Locate and identify every blood parasite.
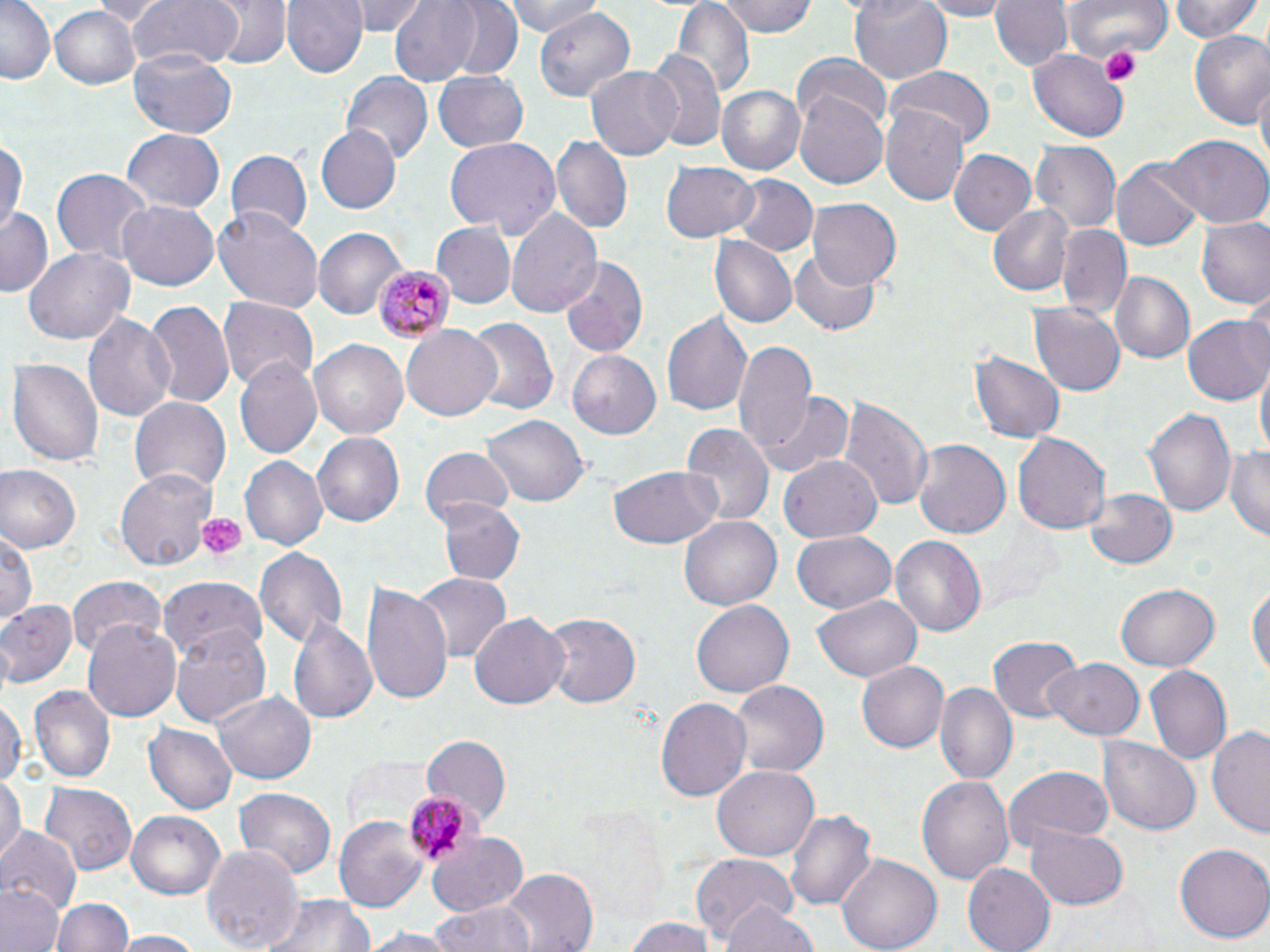

Approximate bounding boxes as (x1, y1, x2, y2) in pixels.
Plasmodium malariae-infected red blood cells: (377, 263, 453, 343), (402, 794, 477, 867).
No Plasmodium falciparum, Plasmodium ovale, Plasmodium vivax, Babesia divergens, or Trypanosoma brucei observed.

Platelet locations: (1100, 45, 1142, 86), (196, 511, 247, 563). Uninfected red blood cell locations: (1, 0, 53, 84), (88, 0, 170, 25), (124, 0, 240, 75), (205, 0, 289, 71), (283, 0, 368, 78), (353, 0, 428, 34), (388, 0, 485, 86), (441, 0, 526, 80), (503, 0, 601, 36), (715, 0, 819, 38), (848, 0, 953, 85), (911, 0, 1016, 18), (991, 0, 1072, 72), (1071, 0, 1171, 62), (1167, 0, 1264, 44), (671, 2, 755, 96), (528, 5, 632, 105), (49, 7, 140, 88), (1187, 27, 1270, 127), (1028, 47, 1128, 140), (128, 50, 236, 137), (647, 51, 725, 155), (792, 52, 889, 133), (585, 68, 682, 159), (888, 69, 994, 148), (433, 72, 527, 153), (341, 73, 432, 168), (1255, 79, 1270, 174), (715, 83, 808, 175), (794, 88, 890, 191), (882, 105, 970, 205), (314, 123, 401, 215), (122, 128, 224, 214), (1160, 134, 1270, 228), (0, 136, 26, 239), (443, 136, 560, 239), (553, 137, 631, 235), (1030, 140, 1121, 235), (949, 148, 1038, 236), (226, 149, 313, 238), (1111, 159, 1204, 248), (660, 162, 757, 243), (51, 168, 151, 263), (729, 175, 816, 255), (118, 200, 219, 292), (807, 200, 902, 291), (989, 203, 1075, 295), (214, 207, 325, 312), (0, 208, 52, 299), (507, 208, 602, 319), (1198, 217, 1270, 310), (432, 221, 514, 308), (1056, 223, 1129, 318), (313, 227, 406, 318), (710, 237, 795, 329), (24, 250, 132, 343), (788, 251, 882, 337), (558, 255, 649, 360), (1111, 272, 1195, 364), (143, 298, 236, 408), (217, 298, 320, 393), (1027, 302, 1126, 395), (659, 307, 753, 420), (82, 311, 176, 423), (1182, 313, 1270, 406), (465, 318, 560, 417), (402, 325, 503, 422), (731, 338, 818, 463), (309, 339, 409, 438), (567, 351, 661, 439), (7, 354, 103, 466), (971, 354, 1065, 442), (233, 356, 323, 462), (1255, 359, 1269, 465), (758, 393, 851, 476), (129, 395, 231, 497), (837, 395, 932, 515), (1143, 407, 1236, 517), (481, 410, 586, 504), (679, 422, 773, 531), (312, 432, 404, 528), (1012, 432, 1109, 535), (911, 440, 1010, 541), (1226, 446, 1270, 542), (420, 448, 515, 527), (780, 455, 882, 542), (240, 456, 327, 550), (609, 462, 726, 550), (0, 464, 81, 552), (115, 467, 216, 569), (1087, 486, 1178, 570), (435, 499, 525, 585), (679, 513, 785, 611), (2, 529, 37, 632), (792, 529, 898, 615), (892, 538, 986, 635), (254, 545, 347, 651), (412, 573, 511, 660), (68, 575, 167, 655), (158, 576, 269, 658), (1248, 576, 1269, 689), (361, 581, 455, 710), (1117, 582, 1219, 671), (811, 593, 923, 682), (0, 600, 77, 685), (691, 600, 792, 700), (469, 612, 568, 712), (542, 612, 640, 708), (289, 613, 381, 727), (82, 619, 182, 722), (168, 624, 273, 729), (989, 636, 1081, 723), (1048, 658, 1146, 741), (858, 660, 949, 753), (1143, 665, 1230, 765), (730, 679, 829, 779), (934, 683, 1018, 786), (29, 685, 116, 783), (213, 688, 317, 785), (0, 693, 24, 792), (654, 696, 753, 802), (145, 721, 240, 815), (1207, 725, 1270, 838), (423, 735, 512, 826), (1099, 736, 1201, 835), (713, 764, 819, 861), (1003, 765, 1113, 853), (916, 772, 1016, 887), (0, 777, 24, 869), (40, 780, 137, 877), (234, 788, 337, 882), (786, 809, 877, 914), (126, 810, 227, 898), (333, 814, 429, 913), (791, 823, 928, 939), (1024, 825, 1129, 908), (0, 829, 81, 915), (425, 832, 529, 914), (1176, 841, 1270, 942), (200, 844, 304, 952), (837, 853, 942, 951), (691, 854, 797, 948), (963, 862, 1055, 952), (498, 868, 599, 952), (0, 881, 64, 952), (55, 894, 130, 952), (256, 894, 374, 952), (432, 900, 539, 952), (719, 902, 822, 952), (626, 916, 722, 952), (355, 927, 463, 950), (113, 931, 203, 952). Slide-level diagnosis: Plasmodium malariae. Optical microscopy. Single field of view. Image is 1270×952 pixels. 1000x magnification. May-Grünwald-Giemsa-stained preparation. Thin blood smear.